State the blood parasite species.
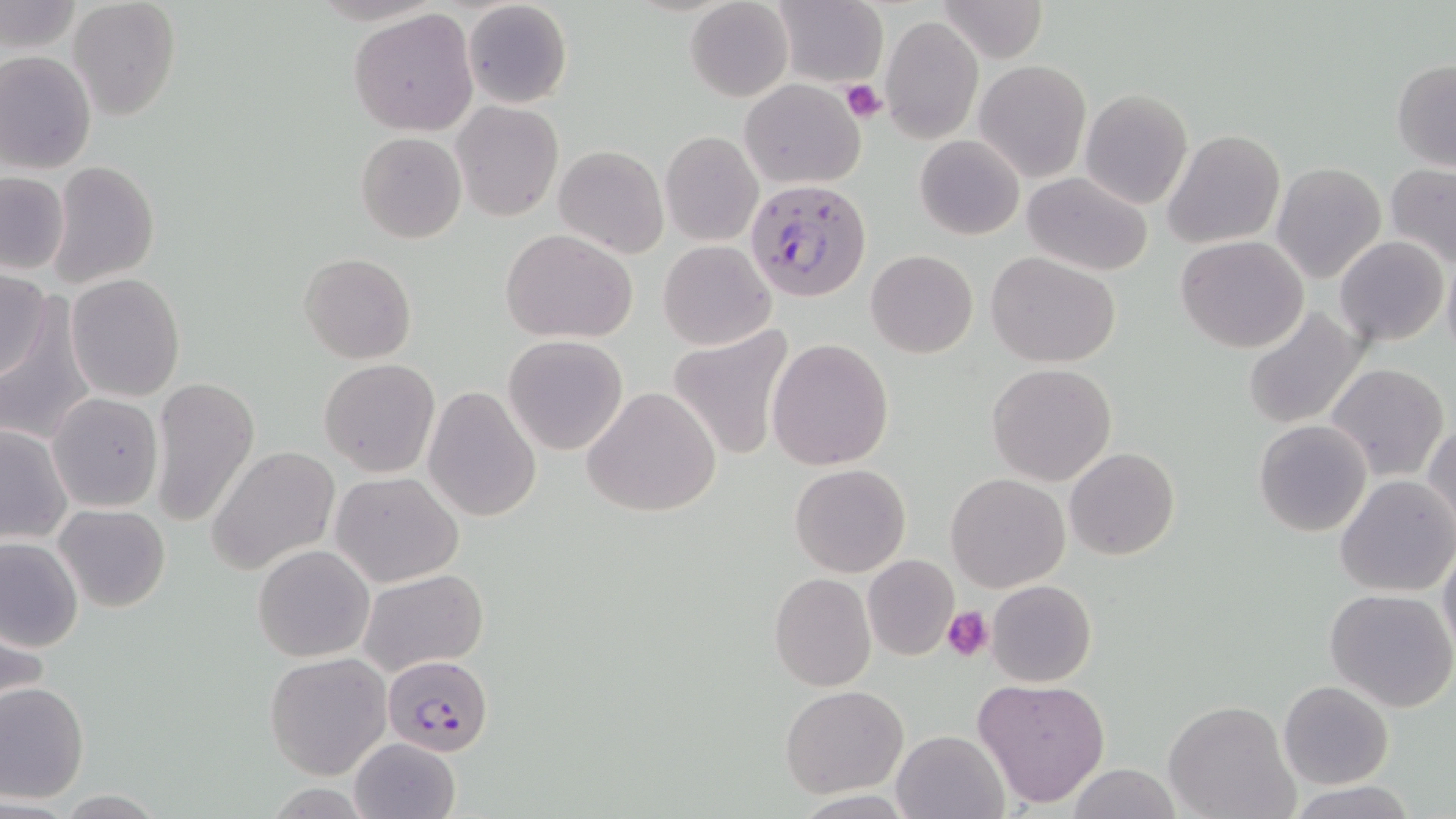
Plasmodium falciparum.

Summary:
  - Coordinate format: approximate bounding boxes as named x1/y1/x2/y2 corners in pixels
  - Uninfected red blood cell locations: (x1=67, y1=0, x2=181, y2=121), (x1=462, y1=0, x2=574, y2=110), (x1=934, y1=0, x2=1051, y2=65), (x1=1, y1=1, x2=80, y2=54), (x1=687, y1=1, x2=791, y2=102), (x1=770, y1=1, x2=886, y2=88), (x1=349, y1=8, x2=478, y2=136), (x1=881, y1=16, x2=984, y2=143), (x1=0, y1=50, x2=97, y2=173), (x1=974, y1=59, x2=1091, y2=182), (x1=1391, y1=60, x2=1456, y2=171), (x1=739, y1=79, x2=865, y2=189), (x1=1080, y1=89, x2=1193, y2=209), (x1=452, y1=101, x2=562, y2=221), (x1=1163, y1=130, x2=1286, y2=249), (x1=355, y1=131, x2=467, y2=244), (x1=660, y1=131, x2=763, y2=246), (x1=915, y1=136, x2=1023, y2=240), (x1=554, y1=144, x2=668, y2=257), (x1=46, y1=160, x2=161, y2=290), (x1=1271, y1=163, x2=1387, y2=284), (x1=1384, y1=163, x2=1456, y2=270), (x1=0, y1=172, x2=70, y2=275), (x1=1020, y1=172, x2=1153, y2=275), (x1=501, y1=228, x2=638, y2=343), (x1=1335, y1=235, x2=1448, y2=347), (x1=1176, y1=236, x2=1310, y2=354), (x1=658, y1=240, x2=776, y2=351), (x1=866, y1=249, x2=978, y2=358), (x1=986, y1=251, x2=1121, y2=368), (x1=298, y1=253, x2=417, y2=364), (x1=1442, y1=253, x2=1456, y2=369), (x1=0, y1=267, x2=52, y2=383), (x1=66, y1=273, x2=185, y2=401), (x1=1, y1=295, x2=94, y2=448), (x1=1241, y1=304, x2=1369, y2=432), (x1=667, y1=325, x2=796, y2=461), (x1=503, y1=335, x2=630, y2=456), (x1=767, y1=338, x2=894, y2=470), (x1=319, y1=358, x2=439, y2=477), (x1=1326, y1=362, x2=1450, y2=483), (x1=986, y1=363, x2=1116, y2=486), (x1=149, y1=376, x2=260, y2=526), (x1=581, y1=385, x2=722, y2=519), (x1=422, y1=386, x2=542, y2=523), (x1=47, y1=392, x2=164, y2=513), (x1=1425, y1=419, x2=1456, y2=536), (x1=1253, y1=420, x2=1373, y2=537), (x1=0, y1=422, x2=73, y2=545), (x1=208, y1=444, x2=339, y2=577), (x1=1065, y1=448, x2=1180, y2=561), (x1=789, y1=463, x2=910, y2=577), (x1=331, y1=472, x2=464, y2=588), (x1=945, y1=473, x2=1070, y2=591), (x1=1334, y1=474, x2=1456, y2=595), (x1=56, y1=504, x2=170, y2=612), (x1=0, y1=535, x2=83, y2=654), (x1=1438, y1=540, x2=1456, y2=659), (x1=253, y1=544, x2=375, y2=662), (x1=862, y1=555, x2=959, y2=662), (x1=359, y1=568, x2=488, y2=676), (x1=769, y1=573, x2=876, y2=691), (x1=987, y1=580, x2=1097, y2=687), (x1=1325, y1=589, x2=1456, y2=713), (x1=265, y1=653, x2=392, y2=780), (x1=972, y1=677, x2=1111, y2=808), (x1=1278, y1=680, x2=1393, y2=789), (x1=1, y1=682, x2=89, y2=803), (x1=781, y1=685, x2=909, y2=797), (x1=1163, y1=700, x2=1300, y2=819), (x1=892, y1=729, x2=1010, y2=819), (x1=350, y1=738, x2=462, y2=819), (x1=1065, y1=764, x2=1180, y2=819), (x1=1282, y1=781, x2=1423, y2=818)
  - Platelet locations: (x1=840, y1=79, x2=887, y2=123), (x1=942, y1=606, x2=993, y2=662)
  - Plasmodium falciparum-infected red blood cell locations: (x1=746, y1=179, x2=872, y2=304), (x1=380, y1=656, x2=495, y2=755)
  - Magnification: 1000x
  - Modality: optical microscopy
  - Field of view: single
  - Preparation: thin blood smear
  - Image size: 1456×819 pixels
  - Stain: May-Grünwald-Giemsa